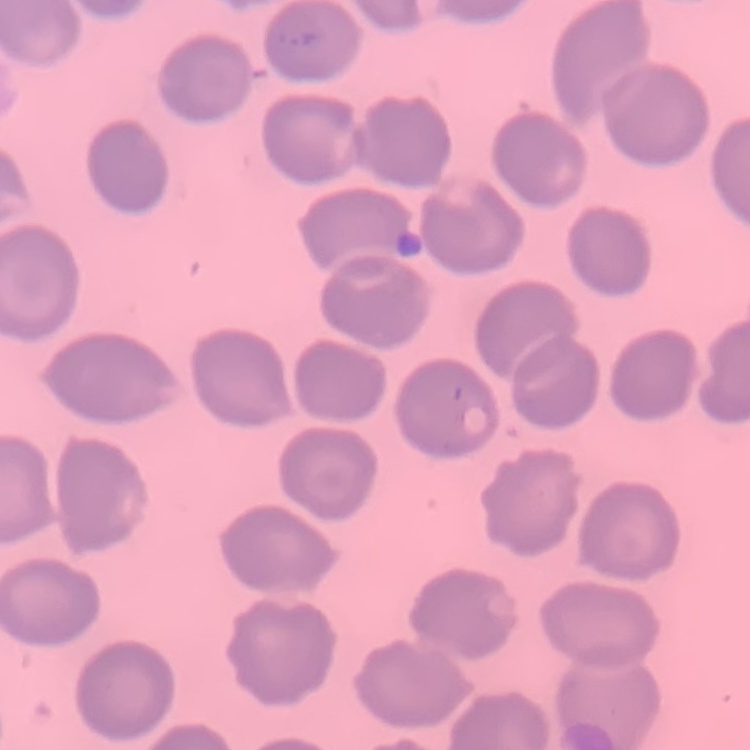

{
  "red_blood_cell_morphology": "no rouleaux formation",
  "preparation": "thin peripheral smear",
  "image_type": "square crop of a larger photomicrograph",
  "stain": "Field's or Giemsa"
}